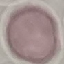

malaria_status: uninfected
image_type: cell patch, automatically extracted from a larger field of view and resized to 64 × 64 pixels
preparation: thin blood film
capture: smartphone through the microscope eyepiece
stain: Giemsa